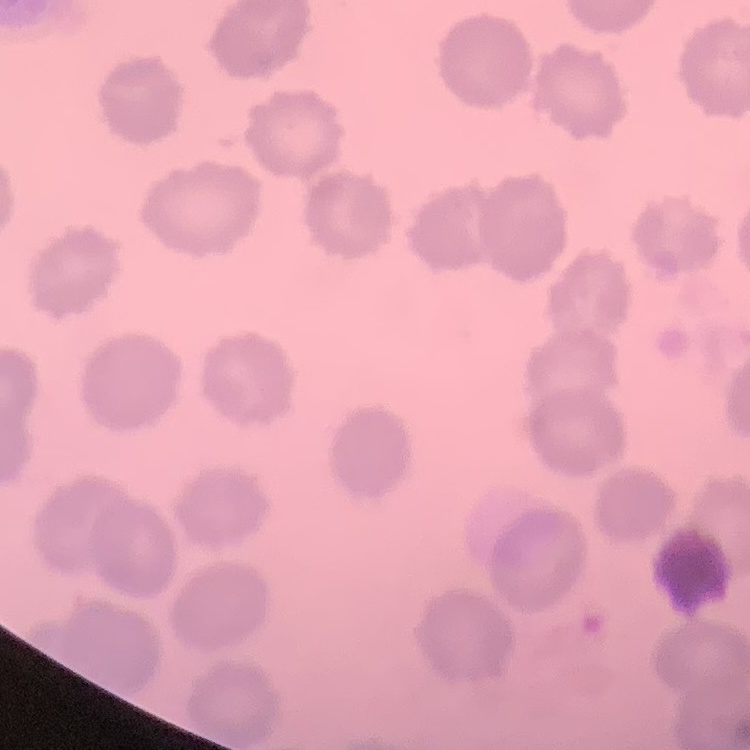 The red blood cells show no rouleaux formation. Thin blood film. One tile cut from a larger photomicrograph. Stained with either Field's or Giemsa.